Draw a bounding box around every Plasmodium parasite, every leukocyte, and every artifact (stain precipitate or debris).
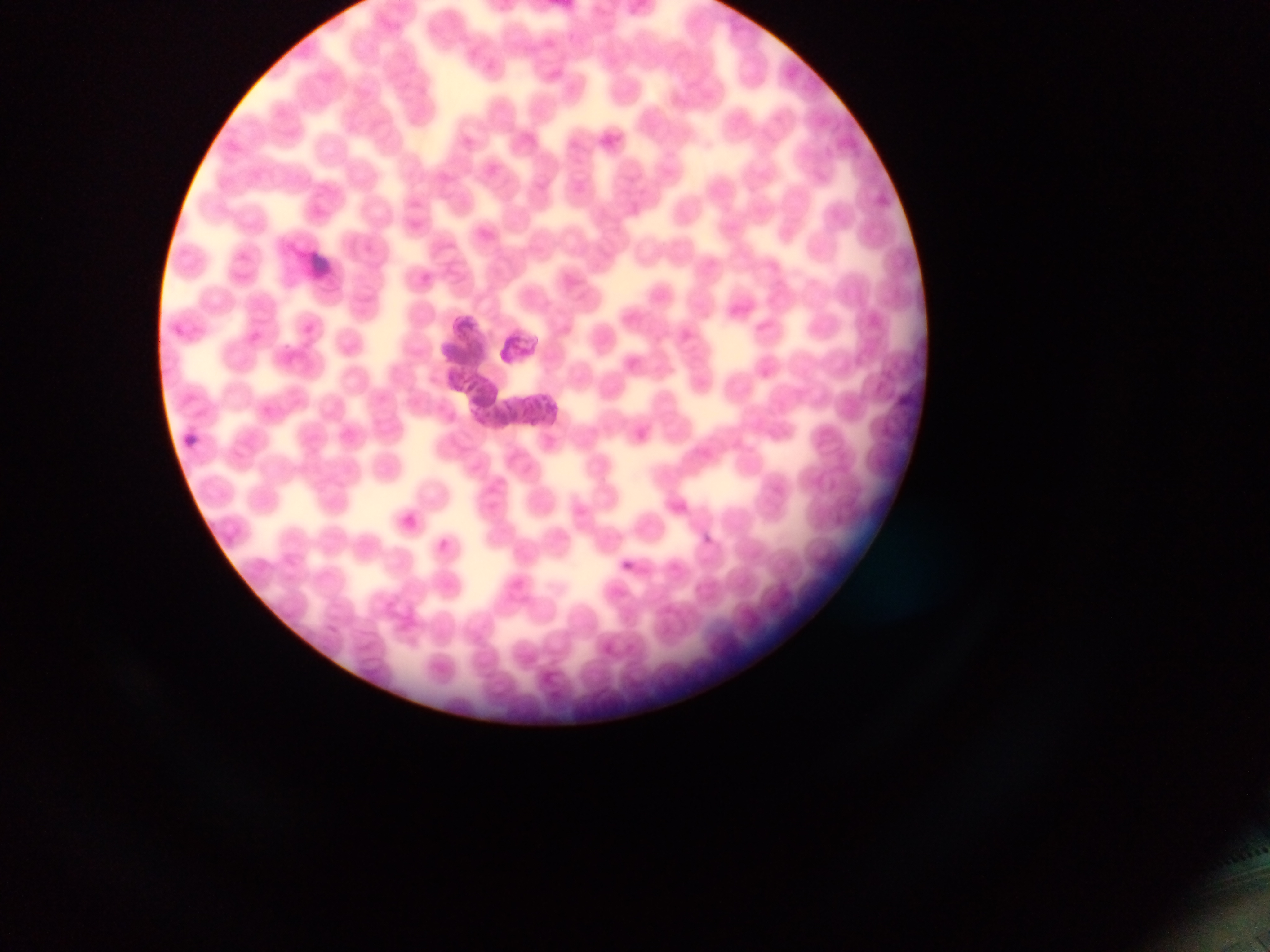

Approximate bounding boxes as {left, top, right, bottom} in pixels.
Plasmodium parasites: {438, 539, 449, 550}.
No leukocytes observed.

Image is 1270×952 pixels. Single field of view. Photographed through a microscope with a mobile-phone camera. Sample from Ghana. Thin blood film.